Outline each blood parasite and name the species.
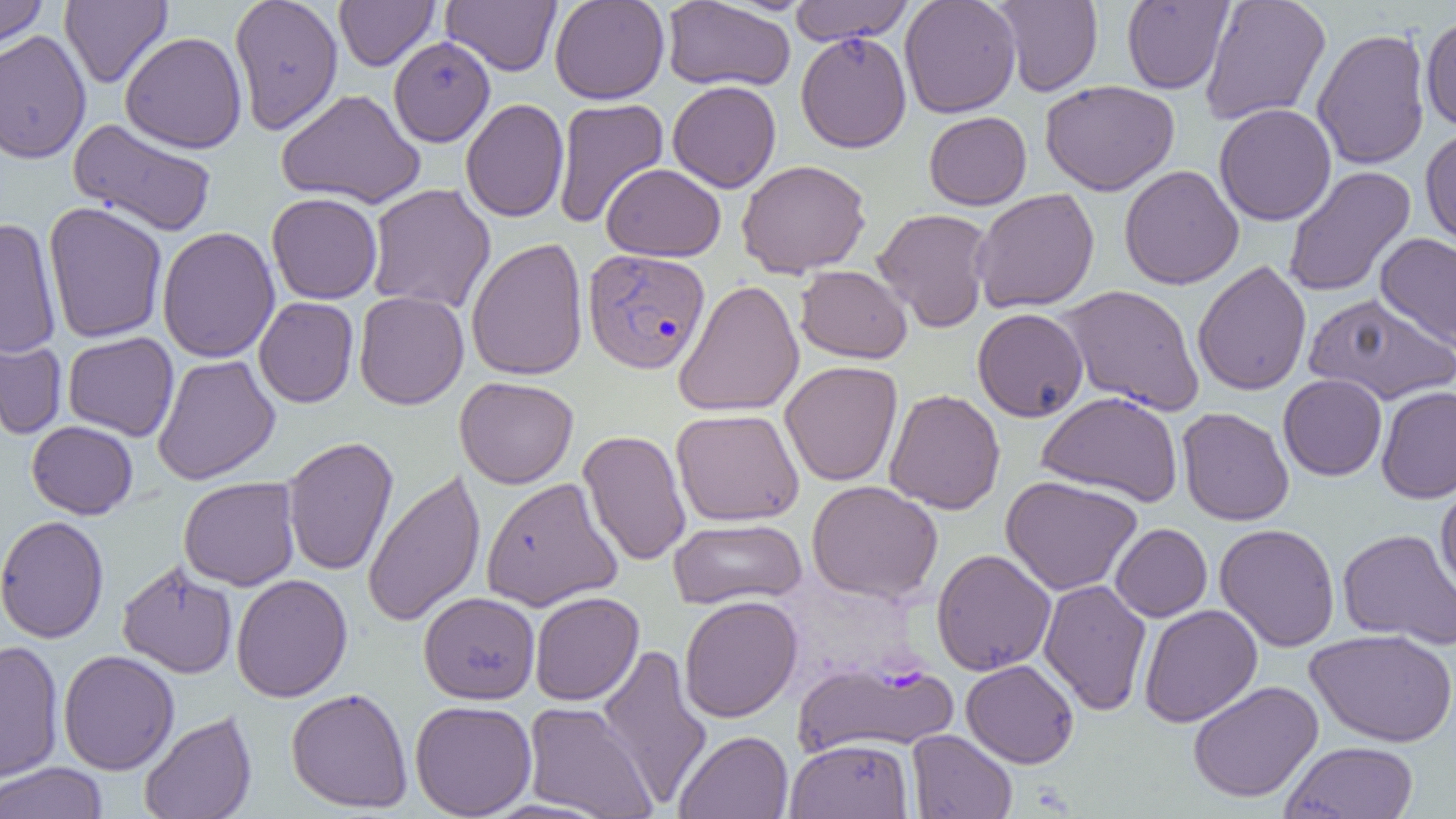

Approximate bounding boxes as named x1/y1/x2/y2 corners in pixels.
Plasmodium vivax-infected red blood cells: (x1=582, y1=248, x2=710, y2=375).
No Plasmodium falciparum, Plasmodium ovale, Plasmodium malariae, Babesia divergens, or Trypanosoma brucei observed.

slide-level diagnosis = Plasmodium vivax
image size = 1456×819 pixels
field of view = single
uninfected red blood cell locations = approximate bounding boxes as named x1/y1/x2/y2 corners in pixels: (x1=0, y1=0, x2=48, y2=52), (x1=59, y1=0, x2=172, y2=88), (x1=229, y1=0, x2=344, y2=135), (x1=334, y1=0, x2=439, y2=71), (x1=441, y1=0, x2=561, y2=76), (x1=549, y1=0, x2=670, y2=104), (x1=789, y1=0, x2=915, y2=45), (x1=899, y1=0, x2=1021, y2=118), (x1=1199, y1=0, x2=1331, y2=126), (x1=662, y1=1, x2=796, y2=92), (x1=992, y1=1, x2=1103, y2=96), (x1=1122, y1=1, x2=1233, y2=94), (x1=1420, y1=16, x2=1456, y2=131), (x1=1312, y1=28, x2=1431, y2=170), (x1=0, y1=30, x2=91, y2=164), (x1=120, y1=31, x2=248, y2=153), (x1=795, y1=31, x2=912, y2=153), (x1=388, y1=35, x2=496, y2=147), (x1=667, y1=80, x2=781, y2=193), (x1=1040, y1=80, x2=1180, y2=196), (x1=276, y1=88, x2=426, y2=209), (x1=552, y1=97, x2=669, y2=229), (x1=460, y1=98, x2=569, y2=223), (x1=1214, y1=103, x2=1337, y2=226), (x1=923, y1=111, x2=1032, y2=210), (x1=68, y1=118, x2=218, y2=237), (x1=1420, y1=126, x2=1456, y2=249), (x1=736, y1=159, x2=871, y2=278), (x1=601, y1=163, x2=726, y2=262), (x1=1119, y1=164, x2=1244, y2=290), (x1=1282, y1=166, x2=1416, y2=298), (x1=366, y1=183, x2=496, y2=315), (x1=971, y1=188, x2=1100, y2=313), (x1=267, y1=192, x2=382, y2=305), (x1=43, y1=202, x2=168, y2=343), (x1=872, y1=207, x2=995, y2=333), (x1=0, y1=217, x2=62, y2=359), (x1=156, y1=226, x2=280, y2=363), (x1=1375, y1=233, x2=1456, y2=351), (x1=465, y1=237, x2=589, y2=382), (x1=1192, y1=260, x2=1312, y2=396), (x1=795, y1=265, x2=912, y2=363), (x1=673, y1=279, x2=804, y2=417), (x1=1057, y1=284, x2=1205, y2=416), (x1=354, y1=291, x2=469, y2=410), (x1=1304, y1=293, x2=1456, y2=405), (x1=254, y1=297, x2=359, y2=407), (x1=972, y1=308, x2=1089, y2=422), (x1=0, y1=324, x2=68, y2=440), (x1=63, y1=332, x2=180, y2=441), (x1=152, y1=354, x2=280, y2=485), (x1=779, y1=361, x2=903, y2=487), (x1=1278, y1=374, x2=1387, y2=481), (x1=454, y1=376, x2=579, y2=489), (x1=1376, y1=386, x2=1456, y2=503), (x1=884, y1=388, x2=1005, y2=514), (x1=1036, y1=391, x2=1184, y2=507), (x1=1177, y1=407, x2=1294, y2=526), (x1=671, y1=408, x2=805, y2=527), (x1=26, y1=420, x2=138, y2=519), (x1=578, y1=429, x2=692, y2=566), (x1=282, y1=436, x2=398, y2=576), (x1=361, y1=468, x2=486, y2=628), (x1=1000, y1=475, x2=1142, y2=596), (x1=1435, y1=476, x2=1456, y2=598), (x1=178, y1=477, x2=301, y2=590), (x1=481, y1=477, x2=623, y2=611), (x1=807, y1=480, x2=944, y2=603), (x1=0, y1=515, x2=109, y2=643), (x1=669, y1=517, x2=807, y2=610), (x1=1110, y1=523, x2=1212, y2=622), (x1=1214, y1=523, x2=1340, y2=652), (x1=1337, y1=528, x2=1456, y2=650), (x1=931, y1=548, x2=1056, y2=675), (x1=117, y1=560, x2=238, y2=679), (x1=231, y1=573, x2=353, y2=702), (x1=1038, y1=579, x2=1152, y2=716), (x1=418, y1=592, x2=540, y2=704), (x1=529, y1=592, x2=644, y2=706), (x1=679, y1=595, x2=803, y2=723), (x1=1139, y1=604, x2=1263, y2=728), (x1=1305, y1=628, x2=1456, y2=747), (x1=0, y1=640, x2=65, y2=783), (x1=597, y1=642, x2=713, y2=809), (x1=58, y1=650, x2=179, y2=775), (x1=793, y1=657, x2=959, y2=759), (x1=961, y1=659, x2=1079, y2=768), (x1=1187, y1=680, x2=1323, y2=803), (x1=286, y1=687, x2=413, y2=813), (x1=410, y1=699, x2=537, y2=818), (x1=522, y1=701, x2=658, y2=818), (x1=139, y1=710, x2=257, y2=819), (x1=906, y1=729, x2=1018, y2=819), (x1=674, y1=730, x2=794, y2=819), (x1=784, y1=739, x2=914, y2=818), (x1=1280, y1=740, x2=1419, y2=819), (x1=0, y1=762, x2=109, y2=819)
magnification = 1000x
preparation = thin blood film
modality = optical microscopy